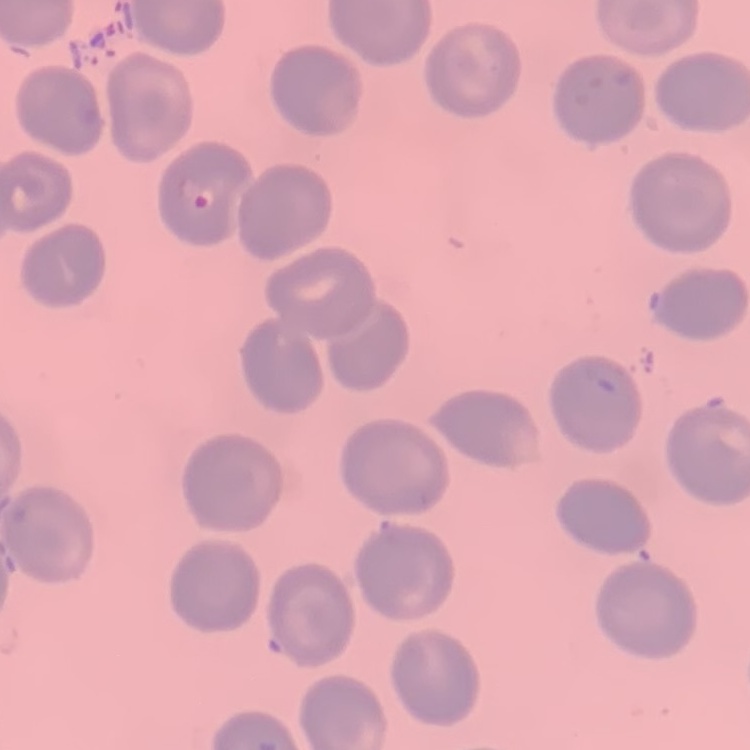 The erythrocytes exhibit no rouleaux formation. Thin blood film. Stained with either Field's or Giemsa. One tile cut from a larger photomicrograph.